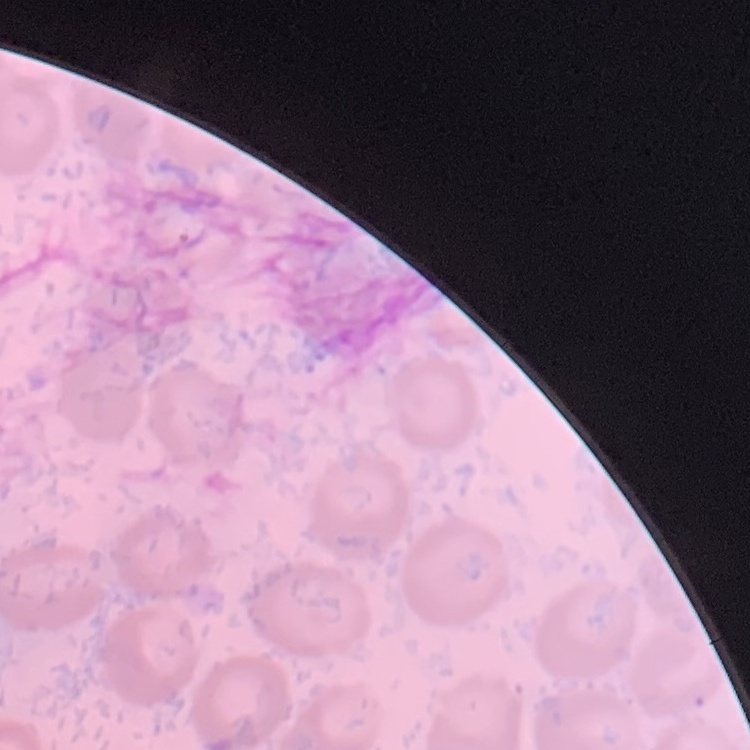
The red blood cells show no rouleaux formation. Thin peripheral smear. Field's or Giemsa stain. One tile cut from a larger photomicrograph.